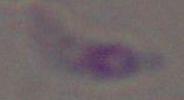
Toxoplasma gondii is shown. 1000x magnification. Photomicrograph.